Point out each malaria parasite.
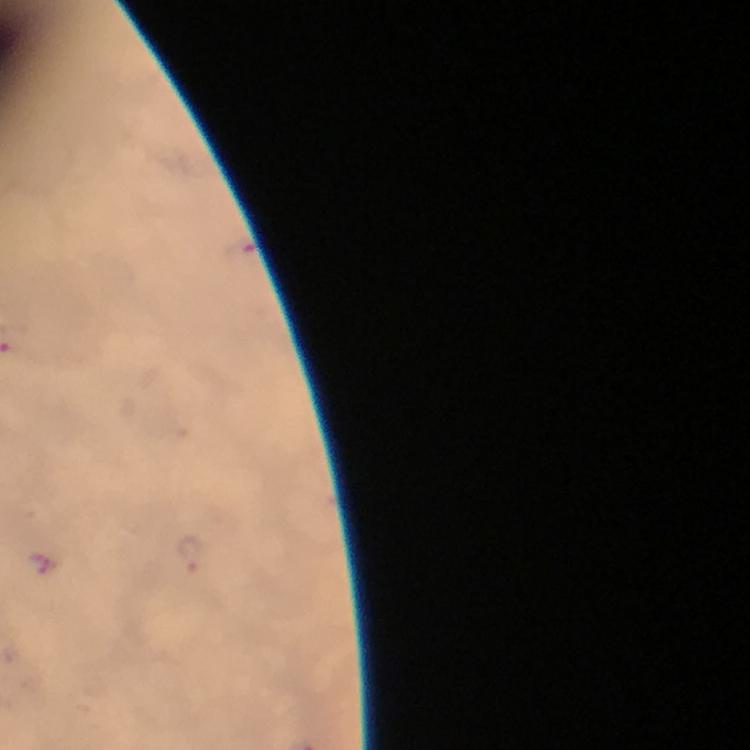
Approximate centers as [x, y] in pixels.
Malaria parasites: [190, 553].

Summary:
  - Preparation: thick blood smear
  - Cropped from: one field of view
  - Stain: Giemsa
  - Context: from a malaria diagnostic workup
  - Magnification: 100x
  - Immersion oil: used
  - Image size: 750×750 pixels
  - Capture: smartphone mounted on the microscope